Assess the morphology of the red blood cells.
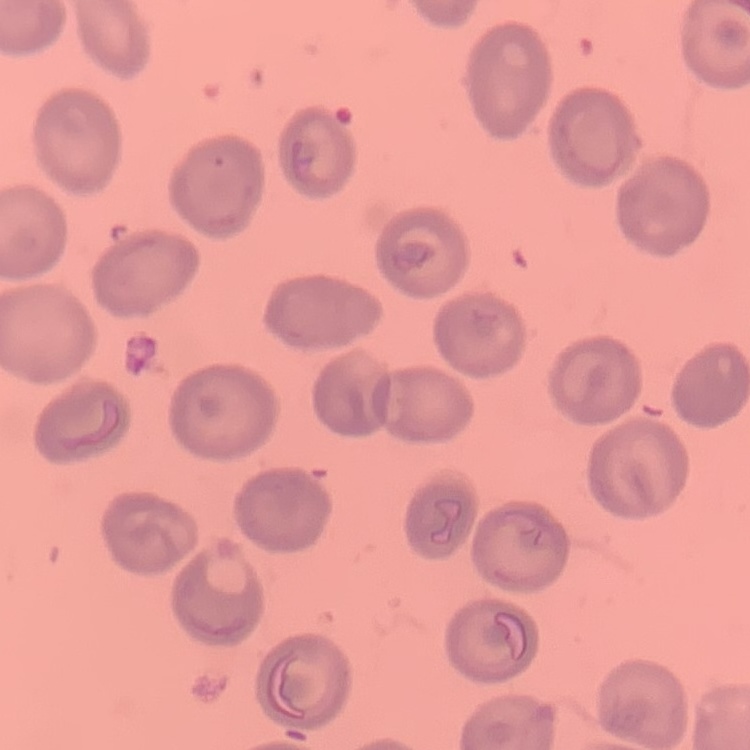

They show no rouleaux formation.

stain = Field's or Giemsa
preparation = thin blood film
image type = one tile cut from a larger photomicrograph